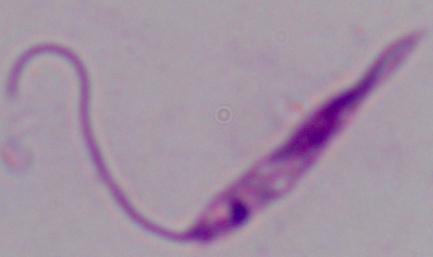
Micrograph. A Leishmania parasite is seen. 1000x magnification.